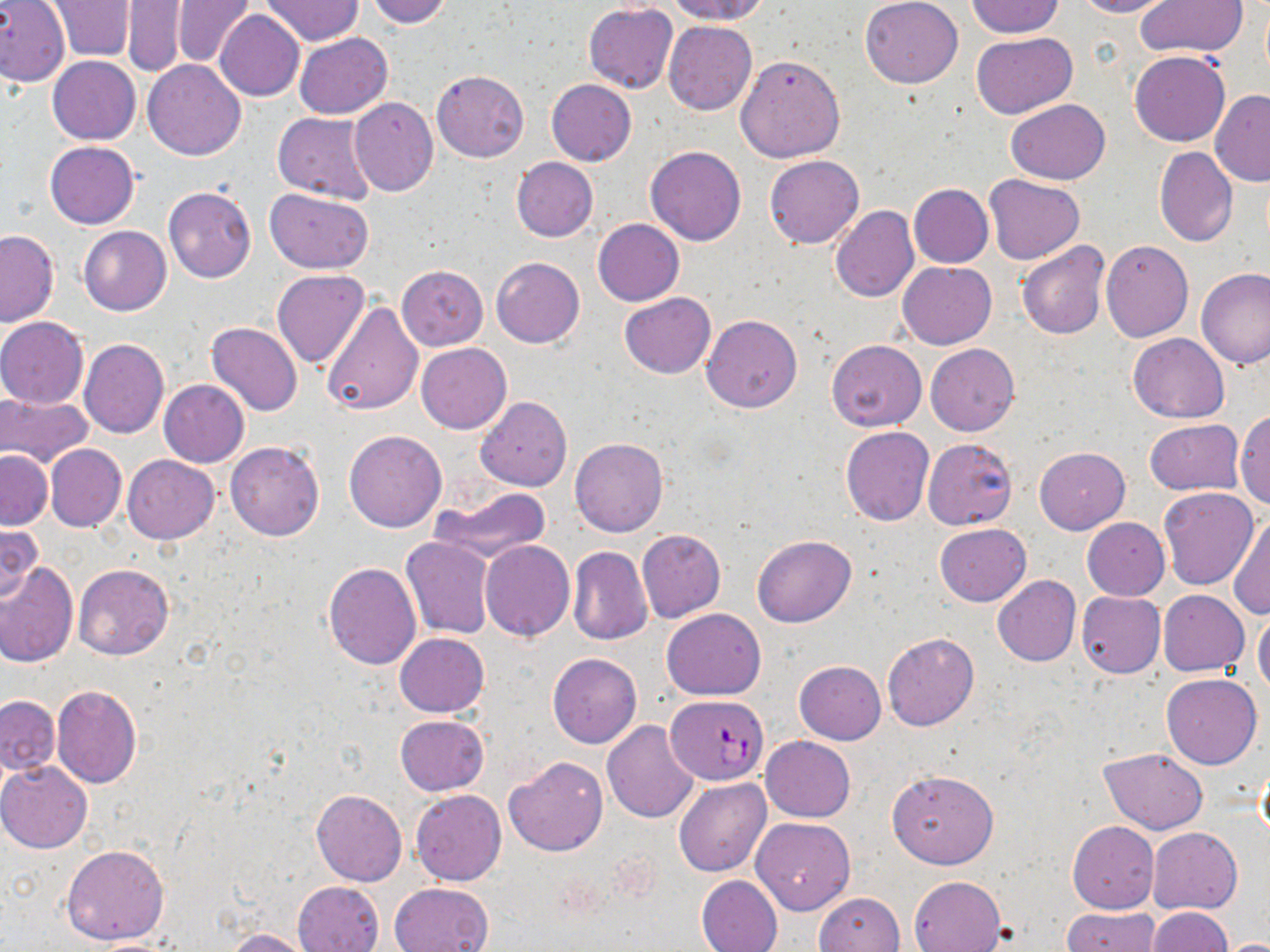

Summary:
  - Coordinate format: approximate bounding boxes as [x1, y1, x2, y2] in pixels
  - Plasmodium falciparum-infected red blood cell locations: [667, 693, 766, 784]
  - Uninfected red blood cell locations: [364, 0, 452, 27], [666, 0, 771, 23], [860, 0, 963, 88], [1072, 0, 1170, 17], [0, 1, 70, 87], [45, 1, 136, 61], [172, 1, 254, 67], [261, 1, 360, 44], [966, 1, 1064, 38], [1137, 1, 1248, 58], [123, 2, 188, 76], [584, 3, 678, 93], [215, 11, 305, 101], [664, 21, 757, 115], [294, 32, 393, 118], [971, 32, 1077, 117], [1131, 51, 1230, 146], [734, 52, 844, 162], [47, 55, 141, 144], [143, 59, 245, 160], [432, 70, 529, 162], [546, 79, 637, 166], [1210, 90, 1270, 187], [348, 97, 437, 197], [1006, 99, 1110, 183], [272, 111, 379, 203], [44, 141, 139, 229], [645, 145, 746, 245], [1154, 147, 1238, 246], [764, 155, 865, 249], [511, 156, 598, 242], [984, 174, 1086, 264], [909, 184, 992, 268], [163, 186, 256, 283], [264, 188, 376, 273], [830, 205, 919, 302], [593, 218, 684, 306], [79, 226, 171, 315], [0, 229, 59, 326], [1100, 239, 1194, 342], [1016, 241, 1109, 340], [491, 257, 584, 347], [899, 262, 996, 349], [396, 266, 487, 350], [1197, 269, 1270, 370], [272, 270, 369, 369], [619, 292, 715, 378], [322, 302, 423, 416], [702, 314, 802, 413], [0, 317, 89, 409], [207, 322, 302, 416], [1128, 333, 1229, 422], [78, 339, 169, 438], [827, 339, 926, 432], [416, 343, 511, 434], [925, 344, 1019, 436], [158, 380, 249, 467], [0, 391, 93, 466], [476, 396, 572, 491], [1233, 411, 1270, 509], [1144, 419, 1243, 495], [841, 427, 934, 526], [344, 429, 448, 532], [570, 438, 668, 537], [922, 438, 1018, 530], [225, 440, 324, 541], [45, 444, 126, 532], [1035, 446, 1130, 534], [1, 450, 52, 529], [123, 455, 219, 544], [432, 486, 551, 563], [1159, 488, 1259, 590], [1230, 510, 1270, 621], [1082, 518, 1169, 600], [0, 523, 42, 606], [934, 524, 1031, 607], [637, 529, 726, 623], [751, 535, 855, 628], [400, 537, 494, 639], [480, 541, 575, 641], [567, 547, 653, 646], [0, 561, 79, 667], [324, 562, 421, 668], [72, 563, 173, 661], [992, 575, 1080, 667], [1158, 590, 1249, 675], [1075, 591, 1166, 678], [661, 608, 766, 700], [1253, 609, 1270, 696], [882, 632, 979, 731], [394, 633, 489, 717], [548, 653, 642, 749], [794, 660, 886, 744], [1161, 674, 1262, 769], [52, 684, 142, 788], [0, 696, 60, 776], [394, 715, 488, 796], [602, 721, 699, 822], [761, 736, 855, 822], [1099, 747, 1208, 833], [504, 755, 608, 856], [1255, 759, 1270, 851], [0, 761, 92, 853], [886, 769, 998, 869], [675, 778, 772, 879], [311, 789, 407, 886], [410, 789, 505, 885], [751, 817, 854, 915], [1068, 822, 1159, 913], [1148, 827, 1242, 913], [61, 844, 170, 946], [696, 875, 783, 952], [908, 875, 1006, 952], [293, 880, 384, 952], [388, 882, 494, 952], [815, 892, 903, 951], [1061, 907, 1159, 952], [1146, 907, 1233, 952], [219, 927, 316, 951], [1211, 937, 1270, 952], [82, 938, 187, 952]
  - Slide-level diagnosis: Plasmodium falciparum
  - Stain: May-Grünwald-Giemsa
  - Field of view: single
  - Magnification: 1000x
  - Modality: light microscopy
  - Preparation: thin blood film
  - Image size: 1270×952 pixels